State which cell type is depicted.
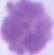
An erythrocyte.

magnification = 1000x
modality = photomicrograph